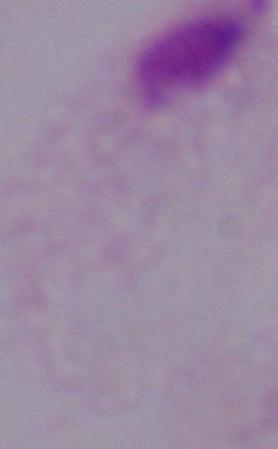

A trichomonad is seen. Micrograph. Captured at 1000x magnification.